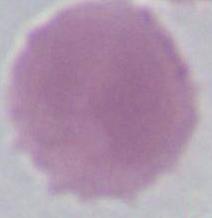
Summary:
  - Modality: micrograph
  - Identification: red blood cell
  - Magnification: 1000x